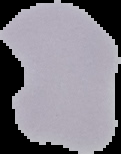
image type = segmented cell region on a black background
image size = 121×154 pixels
result = no malaria parasites detected
preparation = thin blood film